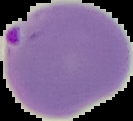 Image is 133×121 pixels. From a thin blood smear. Malaria status: parasitized. The area outside the segmented cell region is set to black.